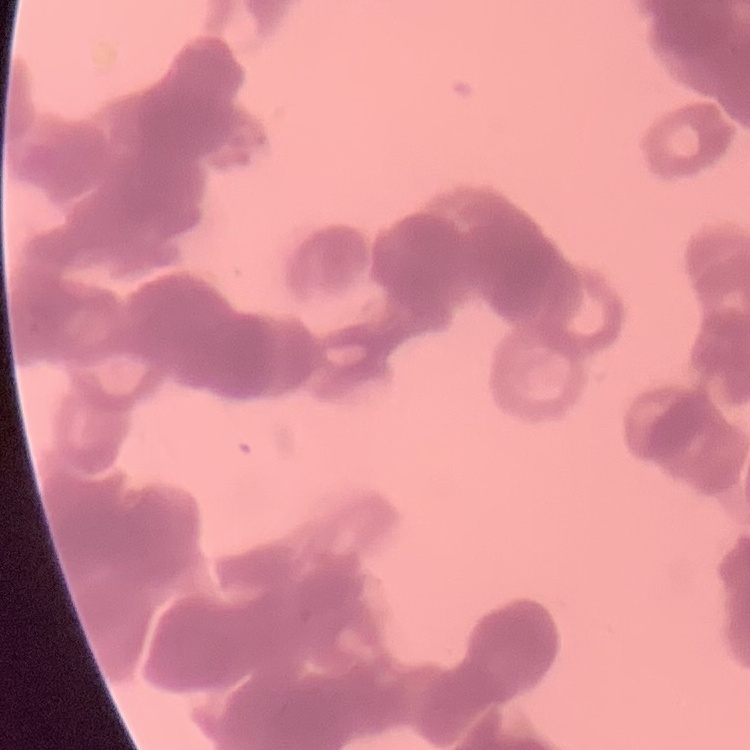
{
  "erythrocyte_morphology": "rouleaux formation",
  "image_type": "square crop of a larger photomicrograph",
  "stain": "Field's or Giemsa",
  "preparation": "thin blood film"
}